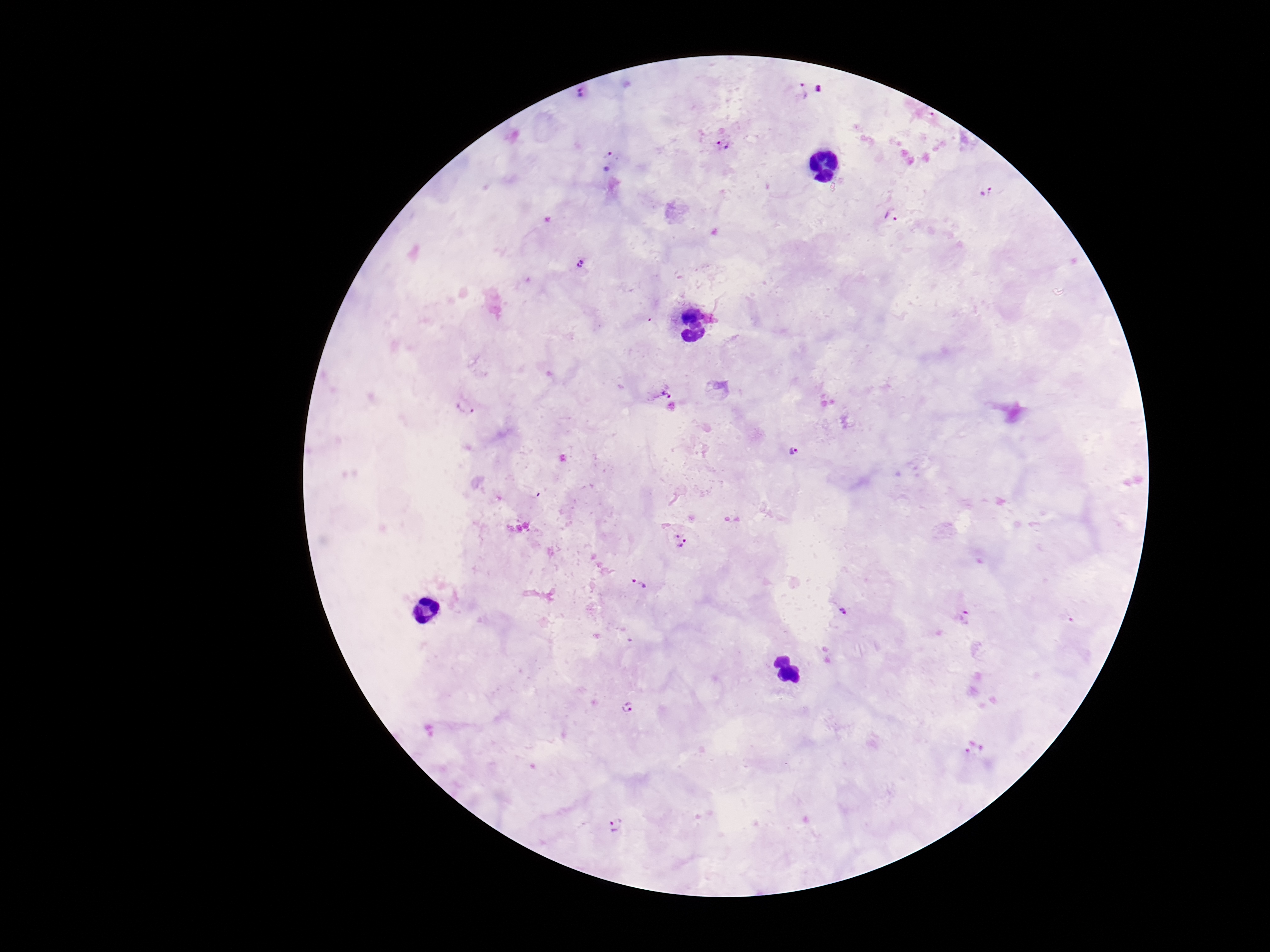
Approximate object centers, in pixels from the top-left corner.
Summary:
  - Plasmodium parasite locations: (x=820, y=90), (x=801, y=91), (x=580, y=93), (x=723, y=146), (x=609, y=156), (x=987, y=191), (x=894, y=217), (x=580, y=263), (x=661, y=390), (x=467, y=406), (x=794, y=452), (x=680, y=541), (x=639, y=584), (x=844, y=611), (x=965, y=618), (x=627, y=707), (x=974, y=747), (x=616, y=825)
  - Preparation: thick blood film
  - Capture: smartphone camera through the microscope eyepiece
  - Image size: 1270×952 pixels
  - Stain: Giemsa
  - Field of view: single
  - Magnification: 100x
  - Patient malaria status: positive